Name the blood parasite species.
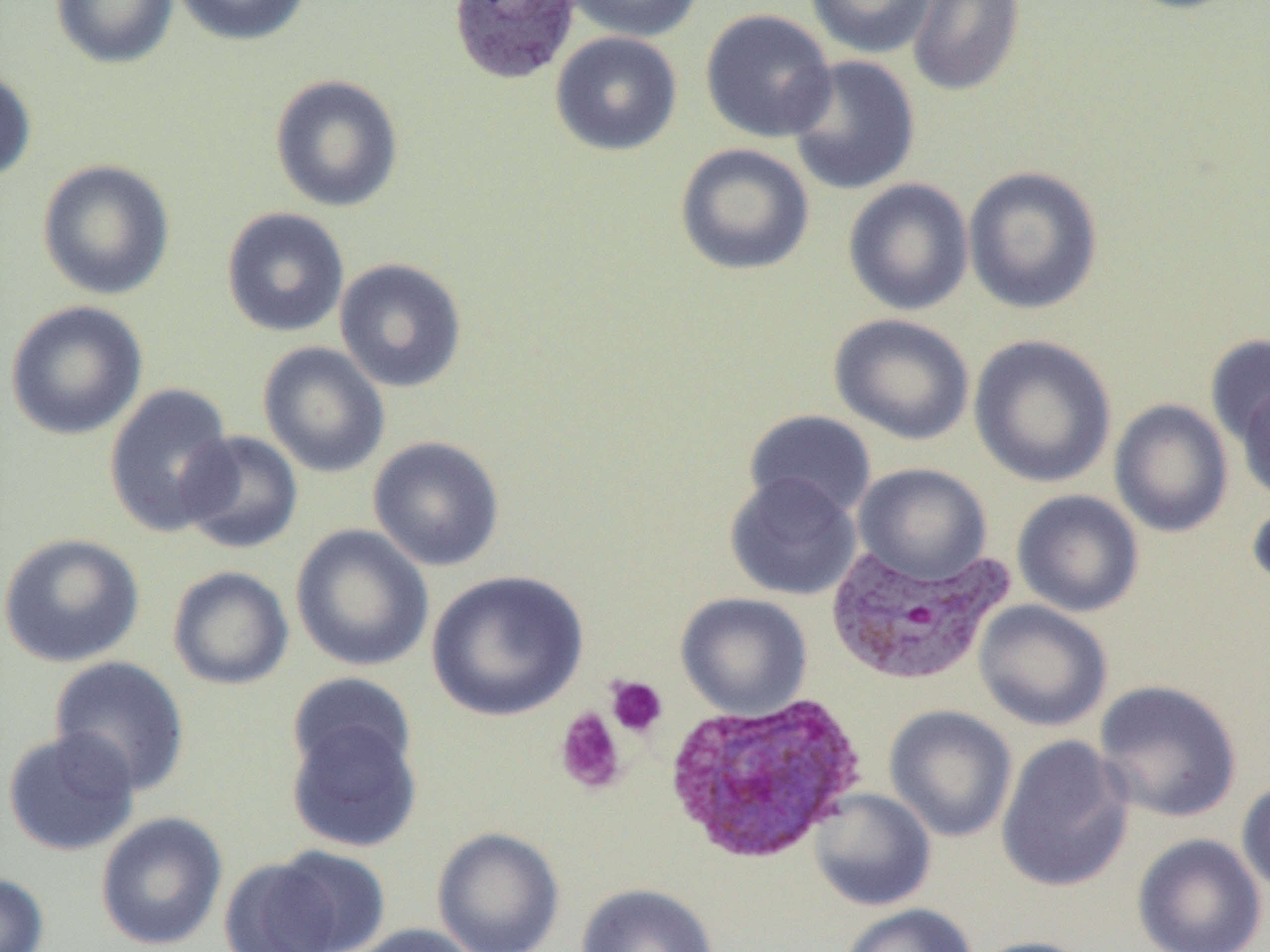
Plasmodium vivax.

{
  "magnification": "1000x",
  "preparation": "thin blood smear",
  "uninfected_red_blood_cell_locations": "approximate bounding boxes as named x1/y1/x2/y2 corners in pixels: (x1=50, y1=0, x2=178, y2=69), (x1=171, y1=0, x2=312, y2=46), (x1=563, y1=0, x2=703, y2=43), (x1=805, y1=0, x2=937, y2=59), (x1=907, y1=0, x2=1026, y2=98), (x1=1116, y1=0, x2=1250, y2=15), (x1=699, y1=9, x2=837, y2=143), (x1=550, y1=31, x2=682, y2=156), (x1=785, y1=55, x2=921, y2=196), (x1=0, y1=67, x2=37, y2=183), (x1=269, y1=74, x2=404, y2=213), (x1=674, y1=143, x2=815, y2=277), (x1=37, y1=159, x2=176, y2=300), (x1=962, y1=165, x2=1104, y2=315), (x1=843, y1=178, x2=974, y2=316), (x1=221, y1=207, x2=350, y2=338), (x1=334, y1=258, x2=468, y2=393), (x1=5, y1=300, x2=148, y2=441), (x1=829, y1=313, x2=976, y2=445), (x1=968, y1=334, x2=1117, y2=488), (x1=1205, y1=334, x2=1270, y2=448), (x1=257, y1=341, x2=390, y2=478), (x1=1235, y1=381, x2=1270, y2=503), (x1=104, y1=382, x2=238, y2=538), (x1=1109, y1=398, x2=1234, y2=538), (x1=743, y1=409, x2=877, y2=521), (x1=178, y1=430, x2=304, y2=554), (x1=368, y1=435, x2=505, y2=572), (x1=854, y1=463, x2=991, y2=584), (x1=724, y1=472, x2=862, y2=601), (x1=1012, y1=489, x2=1144, y2=618), (x1=1247, y1=496, x2=1270, y2=597), (x1=290, y1=524, x2=435, y2=672), (x1=0, y1=532, x2=145, y2=668), (x1=167, y1=565, x2=294, y2=690), (x1=426, y1=570, x2=589, y2=722), (x1=675, y1=591, x2=813, y2=720), (x1=973, y1=600, x2=1113, y2=732), (x1=49, y1=655, x2=191, y2=796), (x1=287, y1=673, x2=417, y2=782), (x1=1093, y1=679, x2=1242, y2=823), (x1=884, y1=705, x2=1018, y2=843), (x1=286, y1=713, x2=422, y2=854), (x1=2, y1=728, x2=141, y2=857), (x1=995, y1=735, x2=1134, y2=893), (x1=1236, y1=777, x2=1270, y2=898), (x1=809, y1=788, x2=936, y2=912), (x1=95, y1=811, x2=228, y2=950), (x1=432, y1=827, x2=565, y2=952), (x1=1131, y1=833, x2=1268, y2=952), (x1=246, y1=845, x2=391, y2=951), (x1=0, y1=873, x2=49, y2=952), (x1=575, y1=882, x2=719, y2=952), (x1=837, y1=903, x2=978, y2=952), (x1=350, y1=922, x2=485, y2=952), (x1=967, y1=936, x2=1100, y2=952)",
  "plasmodium_vivax_infected_red_blood_cell_locations": "approximate bounding boxes as named x1/y1/x2/y2 corners in pixels: (x1=448, y1=0, x2=580, y2=85), (x1=823, y1=540, x2=1015, y2=686), (x1=664, y1=692, x2=868, y2=867)",
  "image_size": "1270×952 pixels",
  "field_of_view": "one of a larger specimen",
  "platelet_locations": "approximate bounding boxes as named x1/y1/x2/y2 corners in pixels: (x1=605, y1=675, x2=668, y2=738), (x1=554, y1=708, x2=627, y2=795)",
  "modality": "light microscopy"
}